Classify this cell by malaria status.
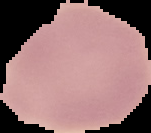
It is uninfected.

{
  "preparation": "thin blood smear",
  "image_type": "segmented cell region on a black background",
  "image_size": "151×133 pixels"
}